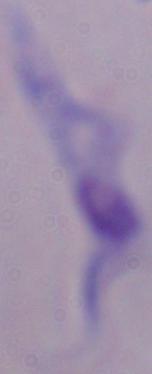

identification = trypanosome
magnification = 1000x
modality = photomicrograph